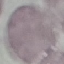
Summary:
  - Malaria status: uninfected
  - Capture: smartphone through the microscope eyepiece
  - Image type: automatically extracted cell patch, resized to 64 × 64 pixels
  - Stain: Giemsa
  - Preparation: thin smear